Name the parasite shown.
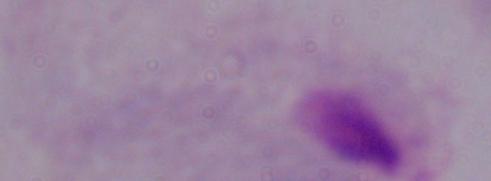
This is a trichomonad.

Captured at 1000x magnification. Micrograph.